Locate every blood parasite and identify its species.
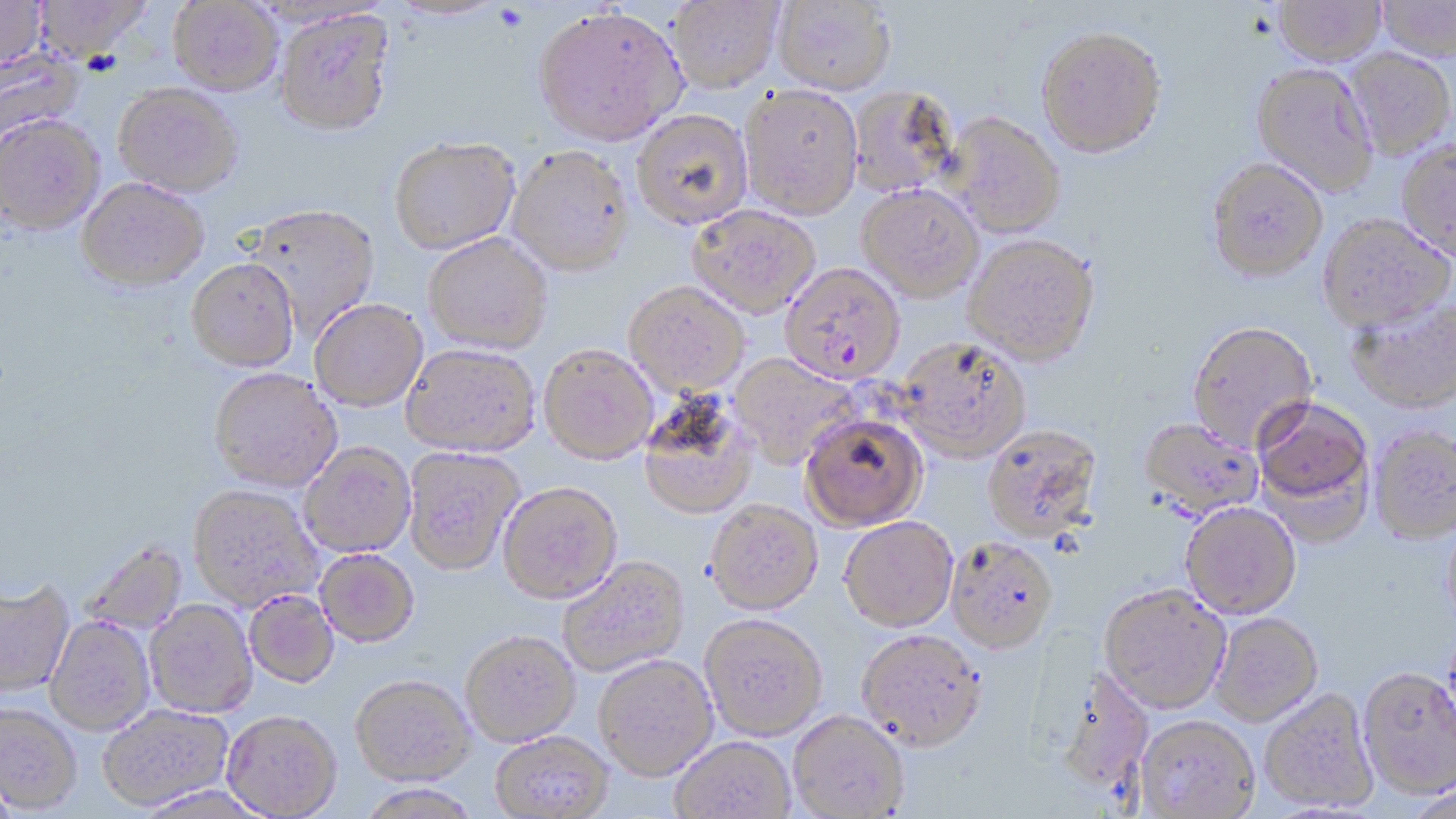

Approximate bounding boxes as (x1, y1, x2, y2) in pixels.
Plasmodium falciparum-infected red blood cells: (780, 263, 905, 385).
No Plasmodium ovale, Plasmodium malariae, Plasmodium vivax, Babesia divergens, or Trypanosoma brucei observed.

Summary:
  - Uninfected red blood cell locations: (0, 0, 47, 73), (34, 0, 154, 62), (666, 0, 785, 96), (1376, 0, 1456, 61), (167, 1, 283, 96), (771, 1, 896, 97), (1272, 1, 1387, 66), (533, 7, 688, 148), (275, 11, 397, 140), (1036, 26, 1167, 158), (0, 46, 84, 146), (1344, 49, 1456, 160), (1251, 62, 1379, 196), (113, 84, 243, 200), (740, 84, 863, 220), (848, 86, 960, 198), (631, 109, 753, 230), (944, 112, 1066, 238), (0, 116, 105, 236), (390, 138, 520, 255), (1396, 138, 1456, 263), (506, 146, 635, 278), (1206, 157, 1329, 281), (76, 179, 209, 294), (857, 184, 984, 301), (687, 204, 820, 318), (245, 205, 381, 341), (1317, 214, 1454, 332), (423, 234, 553, 355), (963, 234, 1100, 366), (186, 260, 299, 374), (624, 282, 750, 397), (1346, 296, 1456, 413), (309, 300, 428, 412), (1186, 320, 1318, 451), (897, 337, 1031, 461), (402, 344, 540, 459), (538, 345, 658, 465), (730, 354, 861, 469), (209, 370, 342, 494), (637, 395, 759, 520), (1252, 396, 1374, 522), (801, 412, 927, 530), (1139, 417, 1263, 520), (982, 424, 1103, 542), (1369, 426, 1456, 543), (299, 443, 416, 559), (403, 447, 525, 576), (498, 482, 622, 604), (188, 486, 322, 612), (704, 499, 824, 614), (1180, 502, 1301, 619), (1442, 513, 1456, 630), (839, 516, 958, 632), (946, 536, 1059, 653), (80, 540, 188, 635), (315, 550, 419, 648), (557, 557, 690, 678), (0, 580, 74, 699), (1099, 582, 1231, 713), (244, 591, 340, 689), (145, 601, 257, 719), (699, 613, 828, 740), (1210, 613, 1323, 725), (46, 617, 156, 736), (856, 629, 987, 750), (460, 631, 581, 746), (593, 654, 718, 780), (1357, 666, 1456, 798), (1051, 667, 1155, 797), (350, 675, 474, 786), (1259, 688, 1378, 813), (0, 703, 81, 814), (97, 704, 233, 811), (788, 710, 910, 818), (222, 712, 342, 819), (1136, 714, 1260, 817), (490, 731, 614, 818), (670, 736, 796, 819), (357, 784, 481, 818), (136, 786, 271, 818)
  - Slide-level diagnosis: Plasmodium falciparum
  - Stain: May-Grünwald-Giemsa
  - Image size: 1456×819 pixels
  - Magnification: 1000x
  - Modality: light microscopy
  - Preparation: thin blood film
  - Field of view: single